Locate and identify every blood parasite.
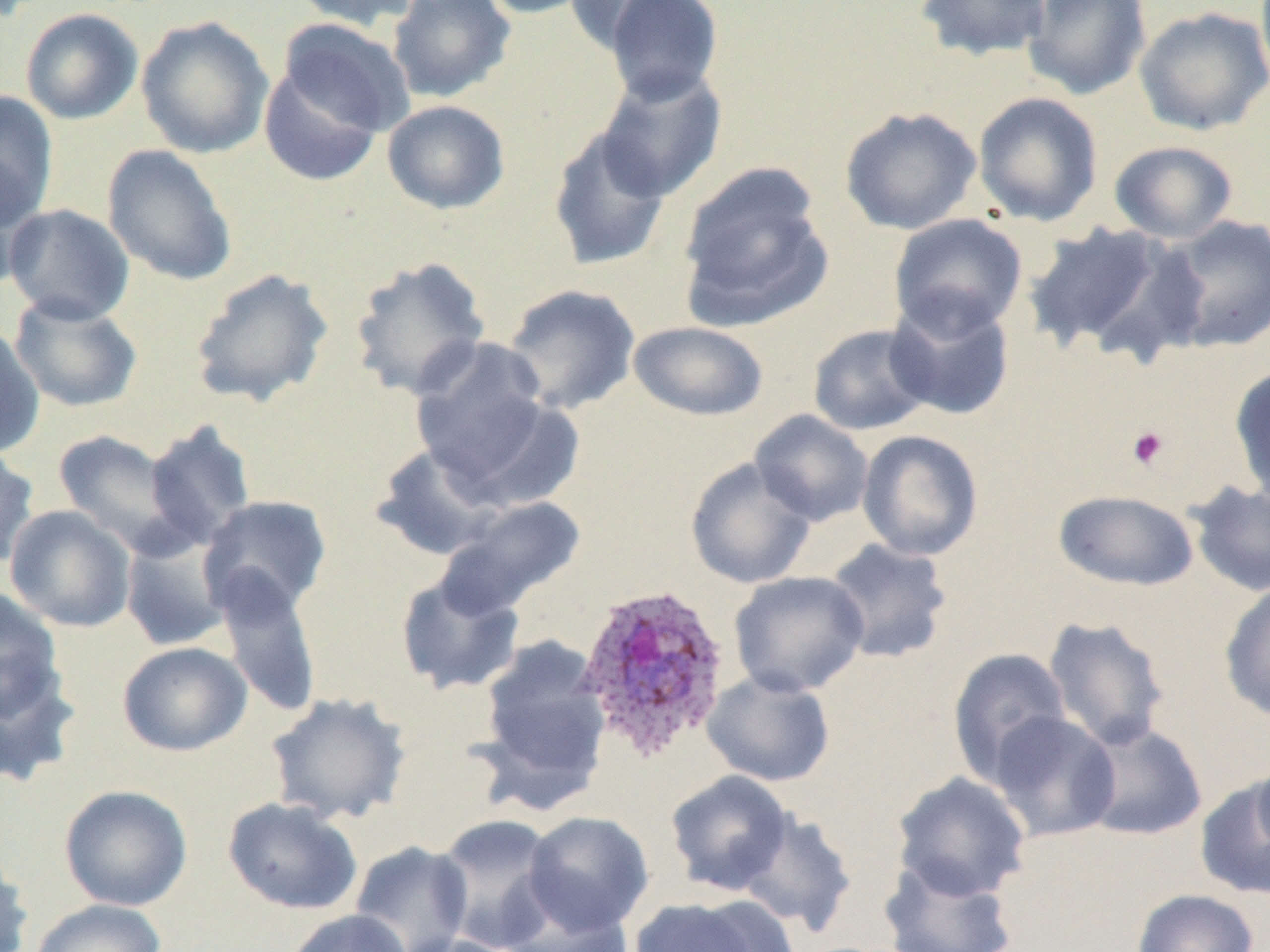
Approximate bounding boxes as named x1/y1/x2/y2 corners in pixels.
Plasmodium ovale-infected red blood cells: (x1=571, y1=585, x2=731, y2=765).
No Plasmodium falciparum, Plasmodium malariae, Plasmodium vivax, Babesia divergens, or Trypanosoma brucei observed.

slide_level_diagnosis: Plasmodium ovale
magnification: 1000x
field_of_view: single
uninfected_red_blood_cell_locations: 'approximate bounding boxes as named x1/y1/x2/y2 corners in pixels: (x1=289, y1=0, x2=424, y2=32), (x1=387, y1=0, x2=516, y2=104), (x1=476, y1=0, x2=598, y2=19), (x1=563, y1=0, x2=691, y2=55), (x1=603, y1=0, x2=725, y2=104), (x1=915, y1=0, x2=1052, y2=62), (x1=1021, y1=0, x2=1152, y2=101), (x1=1134, y1=6, x2=1270, y2=136), (x1=20, y1=8, x2=144, y2=125), (x1=135, y1=15, x2=274, y2=159), (x1=278, y1=19, x2=416, y2=137), (x1=258, y1=63, x2=383, y2=186), (x1=592, y1=67, x2=728, y2=202), (x1=0, y1=91, x2=59, y2=228), (x1=972, y1=92, x2=1104, y2=227), (x1=382, y1=100, x2=510, y2=215), (x1=839, y1=106, x2=982, y2=235), (x1=547, y1=126, x2=672, y2=272), (x1=1109, y1=140, x2=1238, y2=244), (x1=102, y1=144, x2=238, y2=286), (x1=0, y1=160, x2=44, y2=290), (x1=678, y1=164, x2=834, y2=330), (x1=2, y1=204, x2=135, y2=325), (x1=888, y1=213, x2=1027, y2=338), (x1=1162, y1=214, x2=1270, y2=353), (x1=1021, y1=222, x2=1187, y2=359), (x1=349, y1=255, x2=492, y2=401), (x1=188, y1=267, x2=334, y2=408), (x1=502, y1=284, x2=641, y2=416), (x1=8, y1=293, x2=143, y2=412), (x1=884, y1=294, x2=1016, y2=421), (x1=0, y1=321, x2=45, y2=459), (x1=628, y1=321, x2=769, y2=421), (x1=807, y1=323, x2=935, y2=436), (x1=410, y1=338, x2=554, y2=486), (x1=1229, y1=364, x2=1270, y2=507), (x1=443, y1=393, x2=588, y2=511), (x1=750, y1=409, x2=874, y2=526), (x1=143, y1=419, x2=258, y2=550), (x1=52, y1=429, x2=189, y2=556), (x1=857, y1=429, x2=984, y2=561), (x1=369, y1=443, x2=509, y2=562), (x1=0, y1=446, x2=40, y2=570), (x1=684, y1=457, x2=816, y2=589), (x1=1187, y1=481, x2=1270, y2=597), (x1=1053, y1=489, x2=1199, y2=592), (x1=197, y1=495, x2=332, y2=619), (x1=440, y1=496, x2=586, y2=612), (x1=4, y1=504, x2=136, y2=633), (x1=120, y1=530, x2=232, y2=652), (x1=824, y1=538, x2=954, y2=664), (x1=210, y1=567, x2=323, y2=720), (x1=394, y1=571, x2=526, y2=696), (x1=728, y1=571, x2=870, y2=698), (x1=1219, y1=581, x2=1270, y2=723), (x1=0, y1=587, x2=65, y2=723), (x1=1042, y1=616, x2=1172, y2=752), (x1=477, y1=636, x2=611, y2=801), (x1=117, y1=641, x2=252, y2=757), (x1=947, y1=647, x2=1072, y2=787), (x1=0, y1=658, x2=82, y2=789), (x1=702, y1=671, x2=836, y2=787), (x1=265, y1=692, x2=412, y2=825), (x1=988, y1=711, x2=1121, y2=842), (x1=1076, y1=721, x2=1208, y2=841), (x1=1252, y1=750, x2=1270, y2=858), (x1=664, y1=769, x2=794, y2=896), (x1=891, y1=771, x2=1031, y2=902), (x1=1194, y1=778, x2=1270, y2=900), (x1=59, y1=784, x2=193, y2=911), (x1=222, y1=797, x2=364, y2=916), (x1=737, y1=809, x2=857, y2=936), (x1=523, y1=811, x2=654, y2=934), (x1=432, y1=813, x2=563, y2=952), (x1=349, y1=841, x2=473, y2=952), (x1=0, y1=849, x2=33, y2=952), (x1=878, y1=858, x2=1018, y2=952), (x1=1132, y1=889, x2=1260, y2=952), (x1=492, y1=893, x2=638, y2=952), (x1=627, y1=897, x2=773, y2=952), (x1=29, y1=899, x2=167, y2=952), (x1=282, y1=909, x2=413, y2=952), (x1=397, y1=934, x2=519, y2=952)'
modality: optical microscopy
preparation: thin blood film
image_size: 1270×952 pixels
platelet_locations: 'approximate bounding boxes as named x1/y1/x2/y2 corners in pixels: (x1=1126, y1=426, x2=1169, y2=470)'